Locate every Plasmodium vivax-infected red blood cell.
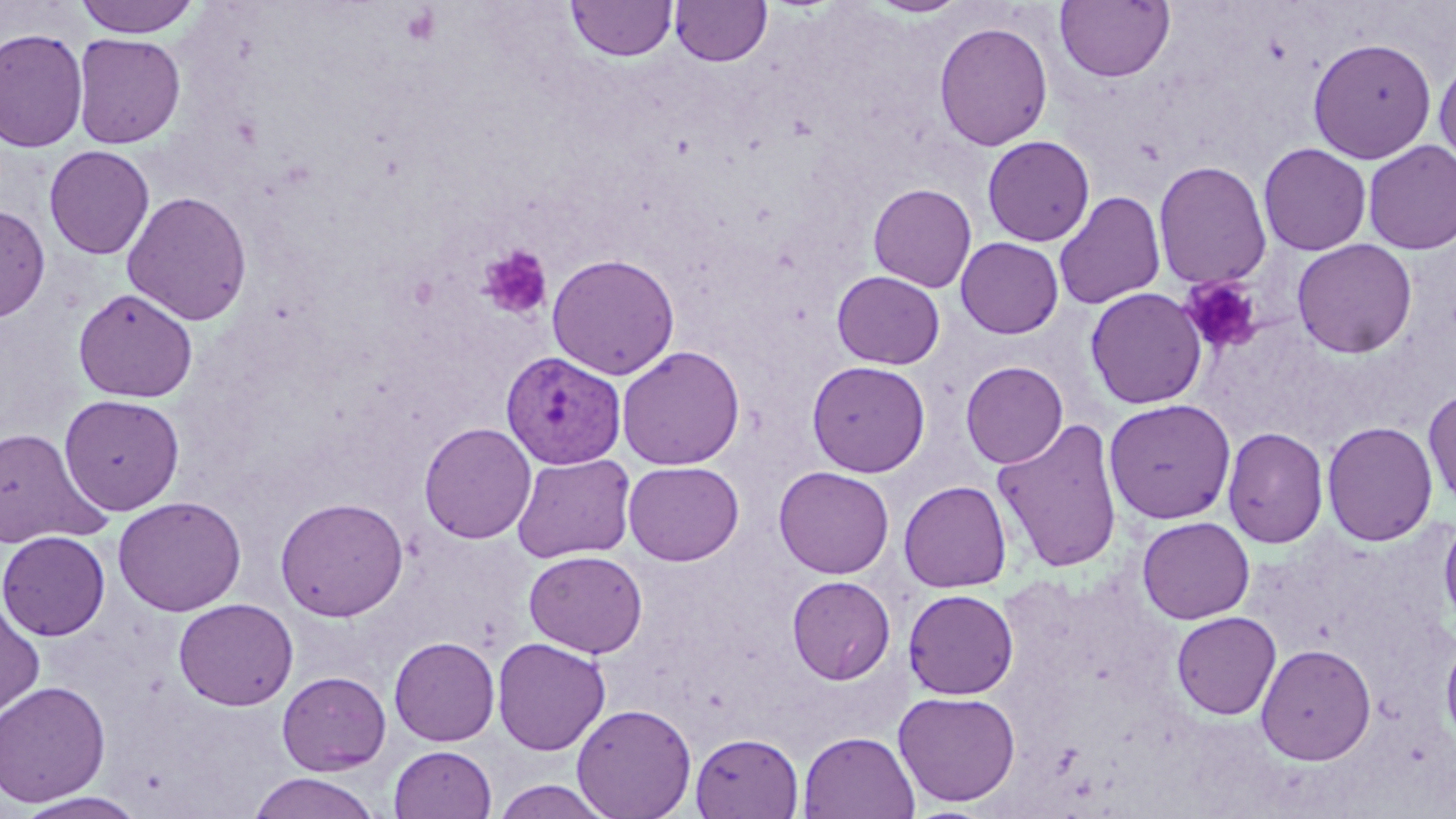

Approximate bounding boxes as (x1, y1, x2, y2) in pixels.
Plasmodium vivax-infected red blood cells: (501, 350, 626, 468).

Summary:
  - Platelet locations: (478, 245, 553, 320), (1180, 276, 1262, 354)
  - Uninfected red blood cell locations: (72, 0, 203, 37), (670, 0, 771, 67), (1055, 0, 1175, 83), (567, 1, 676, 61), (868, 1, 969, 18), (934, 21, 1053, 151), (0, 28, 88, 152), (72, 32, 186, 149), (1307, 37, 1437, 163), (1433, 54, 1456, 173), (982, 135, 1095, 246), (1362, 140, 1456, 254), (1258, 142, 1372, 255), (44, 145, 155, 259), (1153, 160, 1272, 290), (868, 183, 977, 292), (122, 190, 252, 326), (1054, 191, 1166, 310), (0, 205, 50, 323), (955, 237, 1064, 339), (1291, 238, 1417, 359), (546, 253, 680, 379), (832, 271, 945, 369), (73, 287, 198, 402), (1085, 287, 1208, 409), (617, 345, 745, 471), (806, 360, 930, 477), (960, 360, 1068, 469), (1423, 387, 1456, 512), (59, 394, 185, 515), (1103, 398, 1237, 524), (991, 418, 1124, 573), (1321, 421, 1438, 546), (419, 422, 536, 544), (1222, 426, 1329, 548), (0, 427, 108, 550), (512, 453, 636, 563), (623, 461, 744, 566), (774, 466, 894, 578), (898, 480, 1012, 593), (112, 496, 247, 616), (275, 496, 409, 621), (1439, 512, 1456, 632), (1137, 516, 1254, 623), (0, 530, 110, 641), (523, 549, 648, 657), (787, 575, 895, 684), (903, 588, 1019, 699), (0, 596, 45, 724), (173, 598, 298, 711), (1171, 611, 1281, 719), (1440, 631, 1456, 753), (389, 637, 500, 746), (492, 637, 611, 756), (1255, 643, 1377, 765), (276, 671, 391, 775), (0, 680, 111, 807), (893, 690, 1021, 807), (571, 702, 697, 818), (798, 731, 920, 819), (690, 732, 805, 819), (388, 745, 497, 819), (247, 771, 381, 819), (491, 779, 614, 818), (14, 791, 149, 819)
  - Slide-level diagnosis: Plasmodium vivax
  - Preparation: thin blood film
  - Image size: 1456×819 pixels
  - Magnification: 1000x
  - Modality: light microscopy
  - Stain: May-Grünwald-Giemsa
  - Field of view: single